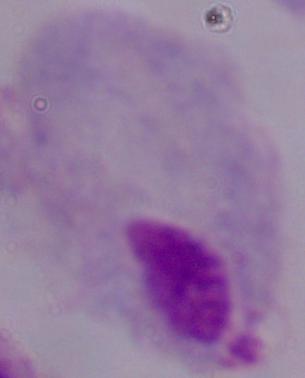

identification = trichomonad
modality = photomicrograph
magnification = 1000x